Name the parasite shown.
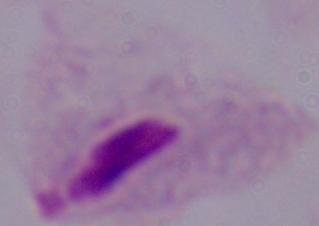
This is a trichomonad.

Micrograph. Captured at 1000x magnification.